Report the malaria status of this cell.
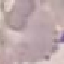
It is uninfected.

Thin smear of blood. Automatically extracted cell patch, resized to 64 × 64 pixels. Giemsa-stained preparation. Acquired by smartphone through the microscope eyepiece.